Give the extent of all Plasmodium falciparum-infected red blood cells.
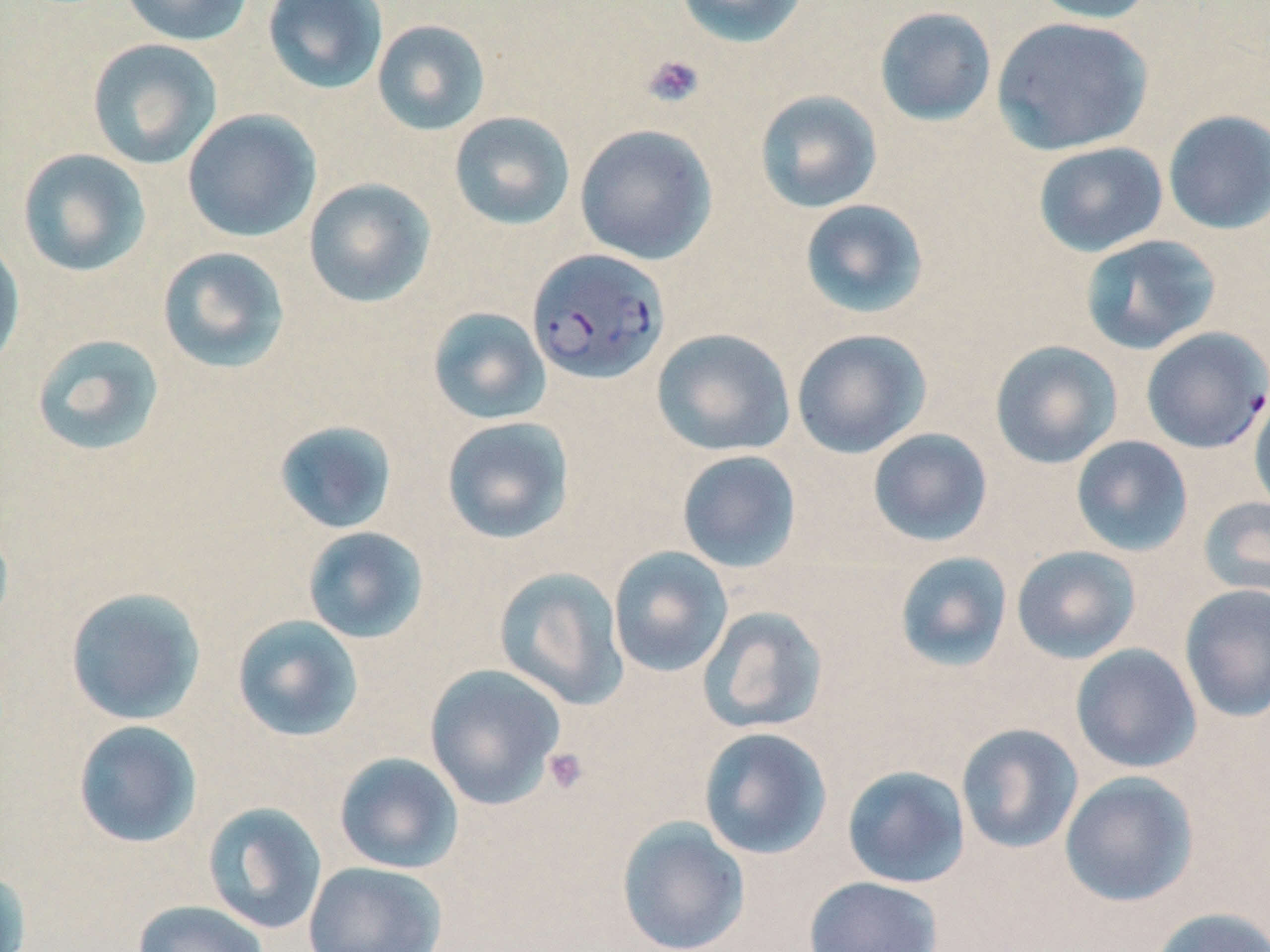
Approximate bounding boxes as [x1, y1, x2, y2] in pixels.
Plasmodium falciparum-infected red blood cells: [527, 248, 669, 384], [1141, 327, 1270, 454].

Uninfected red blood cell locations: [118, 0, 254, 47], [262, 0, 389, 95], [674, 0, 809, 48], [1030, 0, 1157, 24], [873, 6, 997, 127], [991, 16, 1153, 156], [372, 19, 491, 136], [87, 38, 223, 169], [754, 90, 883, 213], [181, 109, 321, 243], [1162, 110, 1270, 235], [448, 111, 576, 231], [574, 124, 717, 265], [1032, 142, 1168, 257], [16, 148, 151, 277], [302, 177, 437, 308], [799, 198, 930, 319], [1079, 234, 1221, 355], [0, 236, 26, 373], [156, 246, 291, 374], [427, 307, 552, 426], [651, 328, 796, 457], [791, 328, 931, 459], [31, 333, 166, 457], [989, 340, 1123, 469], [1248, 390, 1270, 519], [441, 416, 575, 545], [273, 420, 399, 535], [867, 428, 993, 547], [1070, 435, 1194, 557], [676, 450, 802, 573], [1197, 496, 1270, 602], [0, 519, 14, 636], [302, 526, 429, 644], [1011, 545, 1142, 664], [608, 546, 734, 678], [893, 551, 1013, 673], [493, 566, 629, 710], [1179, 584, 1270, 722], [64, 586, 206, 725], [697, 605, 828, 734], [232, 615, 364, 742], [1070, 643, 1202, 774], [424, 663, 567, 809], [72, 720, 203, 849], [956, 723, 1084, 854], [698, 727, 833, 860], [333, 752, 464, 874], [842, 765, 971, 888], [1059, 771, 1200, 907], [202, 801, 328, 935], [616, 816, 751, 952], [303, 861, 448, 952], [0, 867, 31, 952], [803, 876, 943, 952], [132, 900, 269, 952], [1149, 905, 1270, 952]. Platelet locations: [642, 54, 705, 108], [542, 747, 589, 794]. Slide-level diagnosis: Plasmodium falciparum. Image is 1270×952 pixels. Single field of view. Optical microscopy. 1000x magnification. Thin blood film. May-Grünwald-Giemsa-stained preparation.